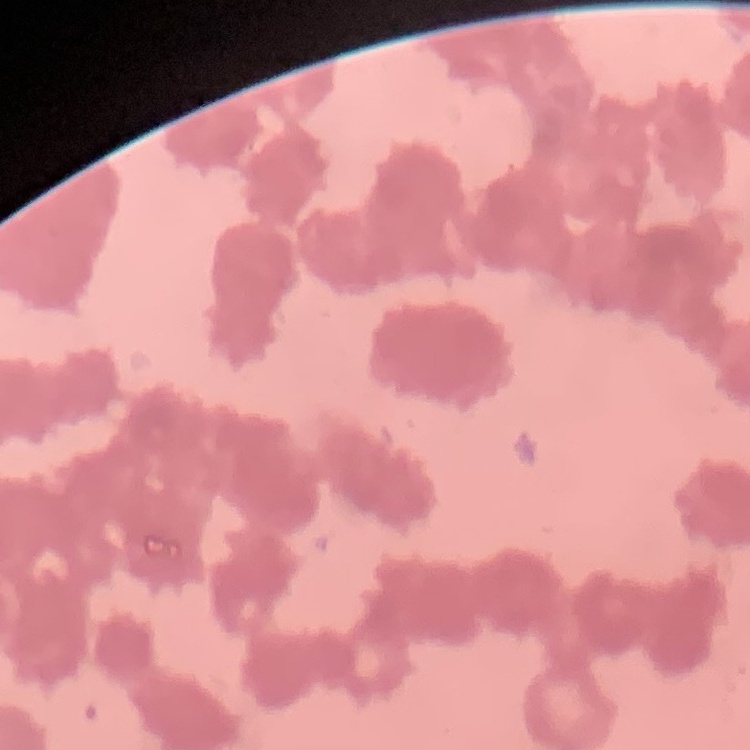
erythrocyte morphology = rouleaux formation
preparation = thin blood film
image type = square crop of a larger photomicrograph
stain = Field's or Giemsa